Look for parasitized red blood cells.
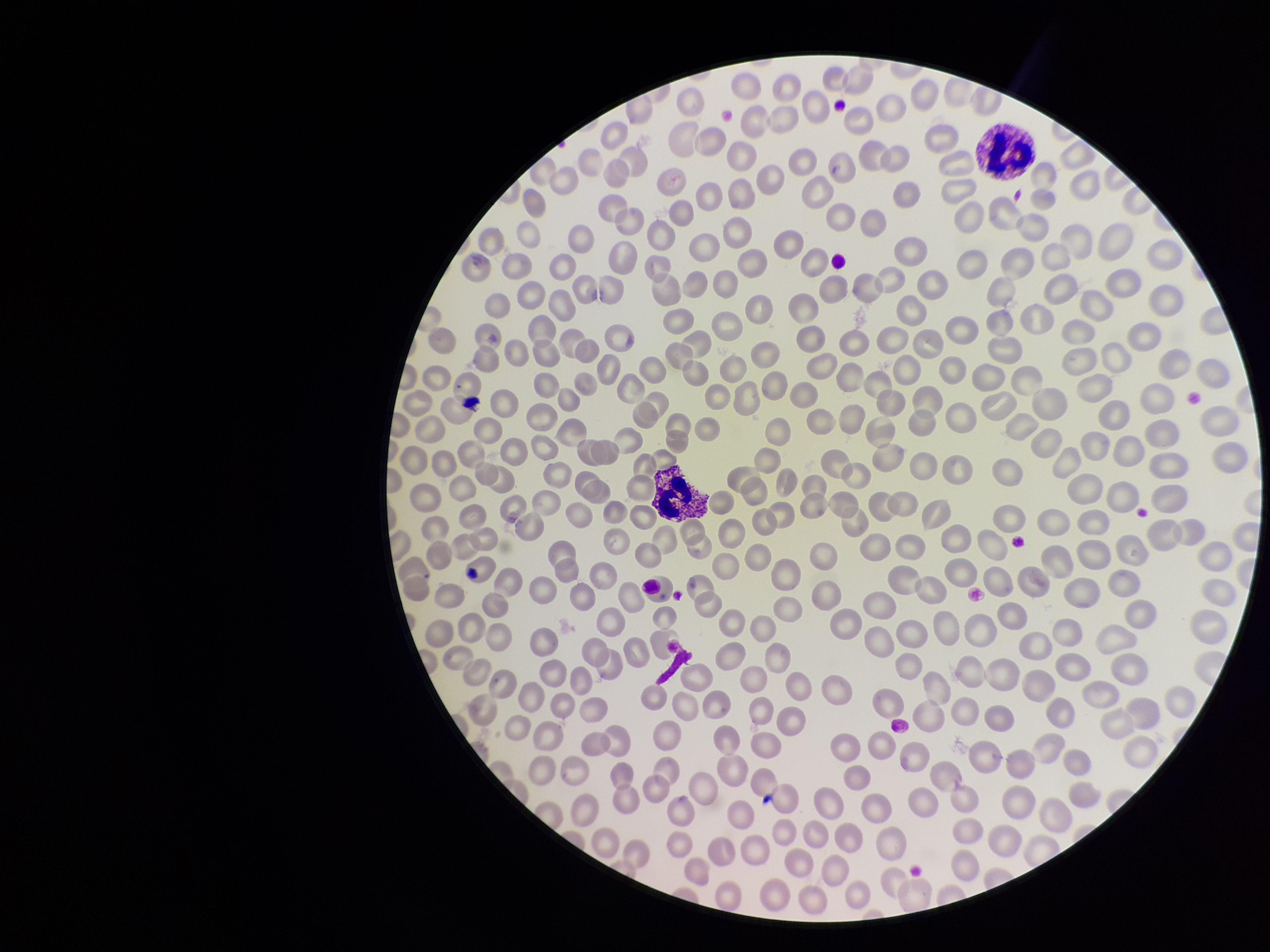

None identified.

Red blood cell count: 235. One field from this slide. Photographed through the microscope eyepiece with a smartphone camera. Patient malaria status: positive. Stained with Giemsa. Species reported for this patient: Plasmodium falciparum. Preparation: thin. Parasitized red blood cell count: 0. Image is 1270×952 pixels.